Classify this cell by malaria status.
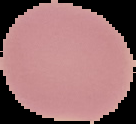
Uninfected.

From a thin blood film. Cell region segmented out of the field of view; the surrounding area is masked to black. Image is 136×124 pixels.